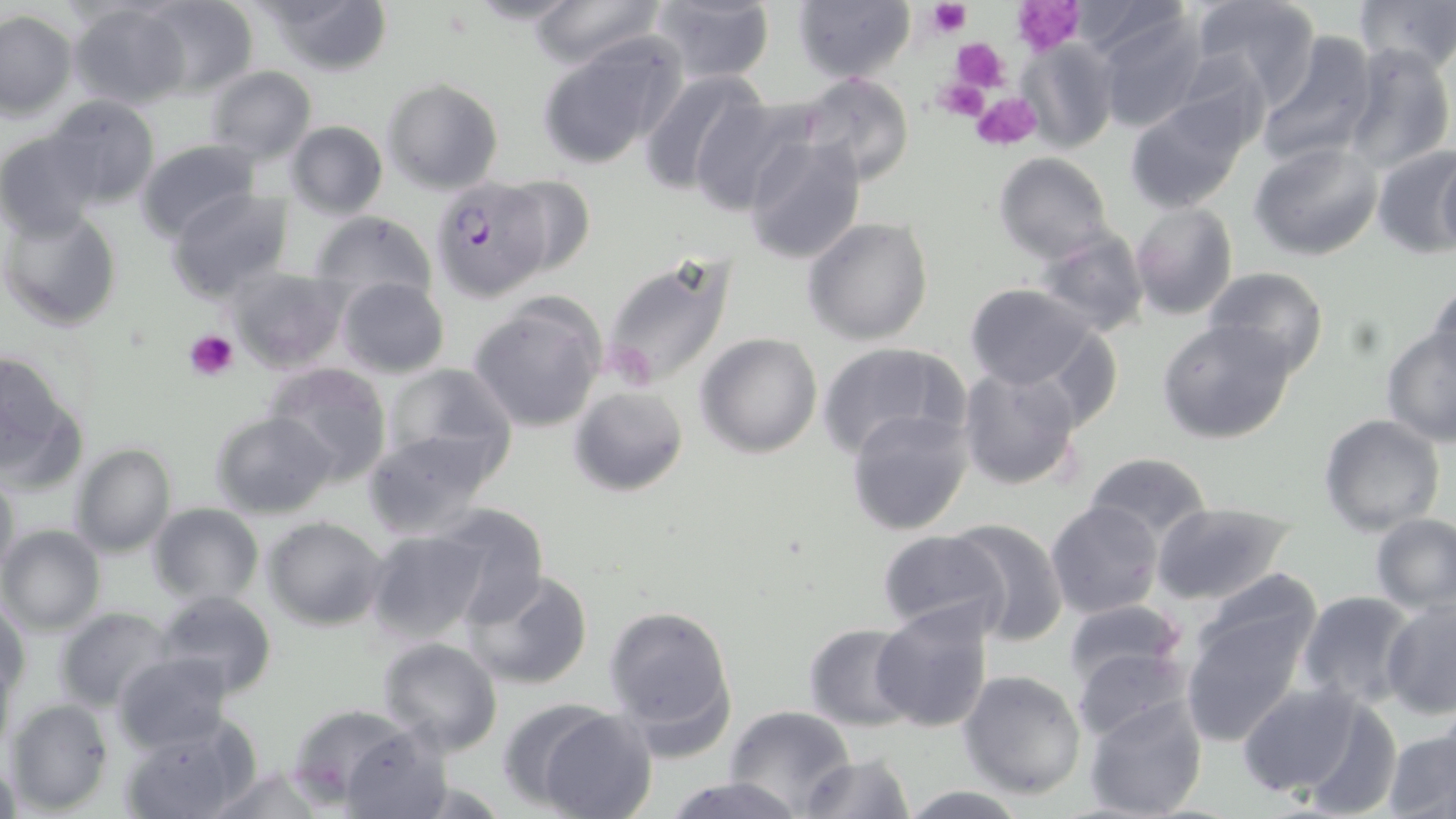
Summary:
  - Coordinate format: approximate bounding boxes as (x1, y1, x2, y2) in pixels
  - Uninfected red blood cell locations: (137, 0, 259, 96), (253, 0, 394, 76), (457, 0, 588, 26), (528, 0, 667, 69), (1187, 0, 1322, 102), (1358, 0, 1456, 74), (68, 1, 188, 110), (644, 1, 777, 85), (790, 1, 915, 85), (1098, 8, 1210, 132), (1, 11, 76, 119), (1254, 30, 1380, 168), (536, 33, 685, 169), (1019, 36, 1116, 154), (1340, 42, 1453, 171), (205, 67, 317, 164), (638, 68, 770, 194), (796, 74, 916, 189), (382, 79, 504, 195), (1123, 93, 1254, 213), (45, 94, 161, 210), (689, 94, 818, 215), (284, 121, 387, 219), (0, 131, 104, 239), (740, 134, 866, 265), (135, 138, 260, 240), (1249, 141, 1384, 261), (1370, 145, 1455, 259), (993, 152, 1113, 263), (1435, 152, 1456, 256), (491, 173, 597, 283), (168, 188, 293, 301), (1128, 202, 1238, 321), (3, 208, 122, 332), (308, 210, 438, 312), (803, 217, 933, 344), (1033, 227, 1150, 338), (598, 248, 740, 395), (226, 268, 349, 372), (1201, 268, 1329, 376), (336, 277, 449, 377), (1426, 281, 1456, 382), (962, 283, 1100, 392), (467, 295, 607, 434), (1156, 318, 1299, 444), (1382, 327, 1456, 445), (696, 333, 823, 458), (815, 341, 969, 461), (0, 351, 85, 489), (262, 361, 393, 485), (379, 363, 518, 478), (957, 364, 1084, 492), (568, 386, 687, 495), (846, 407, 973, 536), (211, 411, 337, 518), (1318, 414, 1444, 535), (363, 430, 501, 540), (69, 444, 174, 557), (1084, 452, 1212, 545), (0, 472, 21, 586), (1045, 500, 1164, 620), (430, 502, 548, 626), (1152, 502, 1296, 606), (147, 504, 263, 604), (1370, 513, 1456, 614), (261, 516, 386, 631), (949, 518, 1068, 645), (1, 525, 105, 635), (364, 529, 489, 647), (875, 529, 1010, 640), (1192, 566, 1326, 677), (464, 569, 594, 691), (153, 591, 277, 699), (1296, 591, 1416, 710), (1380, 596, 1456, 718), (1, 598, 29, 706), (1060, 599, 1189, 700), (602, 602, 737, 751), (872, 602, 995, 733), (54, 606, 174, 711), (1179, 611, 1308, 747), (803, 623, 921, 732), (378, 637, 503, 757), (1070, 643, 1196, 745), (114, 652, 236, 751), (957, 669, 1087, 798), (1236, 681, 1380, 803), (1082, 693, 1209, 818), (5, 699, 113, 815), (722, 706, 857, 814), (529, 708, 657, 819), (288, 711, 446, 814), (117, 717, 258, 819), (1381, 723, 1456, 819), (799, 752, 916, 819), (1, 754, 23, 819), (202, 764, 330, 819), (663, 776, 805, 819), (898, 785, 1029, 818)
  - Plasmodium falciparum-infected red blood cell locations: (428, 176, 556, 298)
  - Platelet locations: (924, 1, 969, 40), (1011, 1, 1084, 54), (952, 39, 1011, 91), (931, 78, 991, 124), (971, 91, 1041, 151), (186, 329, 239, 382)
  - Slide-level diagnosis: Plasmodium falciparum
  - Magnification: 1000x
  - Stain: May-Grünwald-Giemsa
  - Modality: light microscopy
  - Field of view: single
  - Image size: 1456×819 pixels
  - Preparation: thin blood film